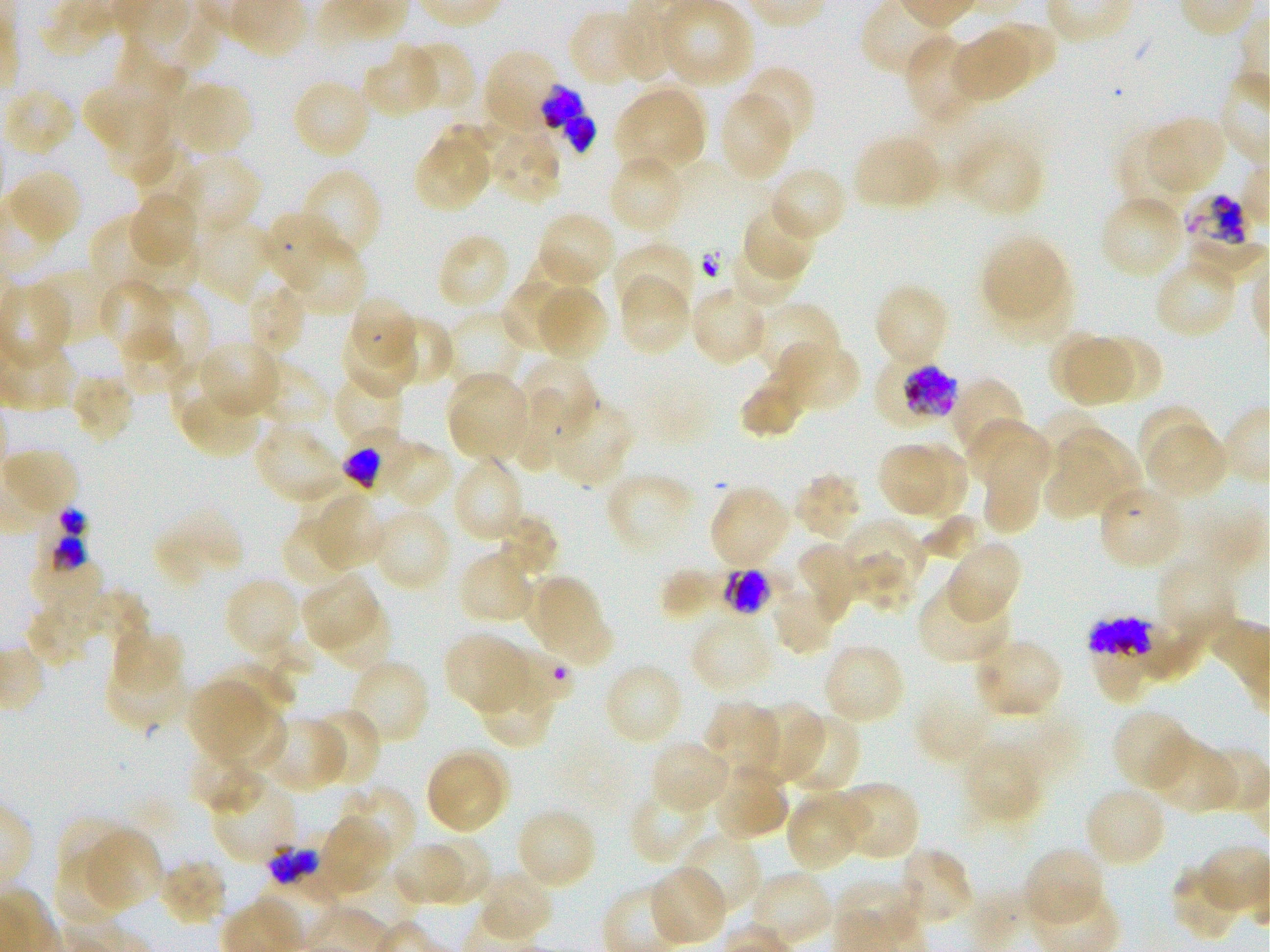 Approximate bounding boxes as (x1, y1, x2, y2) in pixels. Not every red blood cell is marked. A life-cycle stage — or a range of stages, where the recorded stages span more than one — follows each staged infected red blood cell. Locations of infected red blood cells: (541, 84, 597, 153); (876, 357, 961, 429) late trophozoite to early schizont; (342, 431, 407, 492) trophozoite; (38, 507, 89, 571); (722, 568, 772, 617) late trophozoite to early schizont; (1088, 617, 1152, 701) early trophozoite to late schizont. Locations of uninfected red blood cells: (619, 0, 678, 83), (656, 2, 753, 88), (567, 10, 645, 88), (990, 24, 1056, 82), (951, 31, 1033, 102), (904, 35, 978, 123), (116, 38, 187, 119), (405, 39, 476, 113), (362, 48, 440, 119), (484, 49, 562, 134), (738, 65, 816, 147), (291, 78, 372, 160), (173, 82, 253, 156), (84, 83, 171, 154), (615, 86, 707, 173), (3, 87, 76, 158), (719, 92, 794, 181), (914, 104, 996, 190), (1147, 116, 1226, 195), (438, 124, 499, 182), (112, 125, 174, 185), (487, 125, 562, 205), (1115, 127, 1188, 208), (956, 131, 1044, 217), (853, 135, 941, 211), (413, 137, 491, 212), (134, 145, 202, 214), (176, 154, 261, 237), (608, 154, 684, 235), (769, 166, 849, 242), (8, 169, 82, 244), (304, 171, 380, 254), (130, 191, 198, 267), (1099, 194, 1186, 280), (742, 204, 815, 279), (262, 211, 338, 292), (536, 211, 615, 289), (89, 217, 167, 289), (194, 218, 275, 303), (290, 235, 365, 316), (981, 236, 1067, 318), (441, 237, 508, 304), (138, 240, 200, 301), (613, 241, 694, 316), (729, 241, 803, 307), (989, 259, 1074, 342), (1158, 265, 1232, 335), (31, 268, 112, 344), (618, 276, 690, 357), (502, 277, 573, 353), (98, 281, 176, 357), (536, 284, 609, 362), (250, 285, 304, 353), (690, 285, 770, 367), (873, 285, 951, 367), (151, 288, 211, 378), (354, 297, 416, 366), (754, 301, 841, 382), (445, 311, 526, 388), (384, 316, 455, 388), (346, 324, 417, 399), (125, 326, 186, 392), (1050, 332, 1117, 398), (1097, 335, 1161, 400), (1064, 339, 1133, 406), (199, 340, 282, 418), (779, 340, 859, 413), (521, 357, 598, 440), (168, 358, 232, 425), (256, 362, 330, 433), (333, 371, 406, 446), (446, 371, 530, 459), (70, 373, 136, 444), (739, 373, 806, 439), (950, 377, 1026, 461), (450, 387, 522, 456), (184, 395, 260, 454), (552, 399, 634, 487), (1135, 403, 1212, 476), (1040, 408, 1108, 479), (969, 419, 1049, 484), (1147, 422, 1227, 500), (255, 424, 343, 504), (1056, 430, 1143, 515), (981, 439, 1041, 537), (384, 441, 455, 509), (911, 443, 969, 521), (879, 445, 945, 515), (4, 447, 80, 519), (1043, 447, 1119, 521), (453, 455, 526, 543), (604, 472, 694, 556), (793, 473, 863, 541), (709, 485, 791, 568), (1099, 488, 1183, 565), (313, 492, 388, 569), (159, 505, 242, 579), (371, 508, 452, 592), (281, 514, 355, 588), (493, 514, 558, 580), (920, 514, 982, 562), (840, 517, 925, 601), (152, 531, 208, 590), (946, 540, 1023, 621), (793, 542, 857, 622), (458, 548, 536, 626), (852, 550, 917, 615), (1154, 555, 1238, 646), (659, 568, 722, 619), (526, 574, 610, 665), (223, 576, 300, 660), (301, 576, 379, 652), (917, 582, 1011, 665), (771, 585, 839, 656), (85, 589, 149, 651), (24, 602, 93, 668), (1141, 616, 1209, 684), (690, 617, 775, 694), (112, 626, 186, 693), (442, 632, 528, 715), (973, 636, 1065, 719), (256, 638, 315, 704), (821, 643, 906, 726), (345, 657, 431, 747), (103, 659, 189, 730), (213, 661, 295, 722), (603, 661, 684, 747), (478, 672, 556, 750), (186, 680, 264, 760), (913, 687, 991, 765), (750, 698, 823, 784), (213, 701, 287, 773), (703, 702, 781, 784), (310, 707, 384, 788), (1111, 708, 1194, 792), (784, 713, 862, 796), (266, 716, 347, 793), (1149, 737, 1237, 816), (649, 739, 731, 814), (961, 740, 1042, 823), (187, 747, 264, 813), (1201, 747, 1270, 814), (439, 748, 510, 819), (425, 756, 503, 833), (715, 763, 788, 841), (211, 776, 297, 865), (837, 781, 921, 862), (338, 784, 418, 866), (1083, 785, 1166, 868), (628, 788, 709, 866), (785, 791, 865, 871), (515, 808, 598, 889), (55, 815, 133, 890), (318, 816, 391, 893), (83, 828, 163, 911), (680, 832, 762, 917), (422, 835, 491, 904), (392, 840, 466, 908), (896, 847, 975, 928), (1023, 847, 1106, 926), (54, 849, 127, 927), (158, 857, 228, 926), (1171, 863, 1243, 940), (649, 865, 730, 947), (483, 871, 557, 938), (749, 871, 834, 947). Locations of red blood cells of indeterminate infection status: (1182, 192, 1248, 248), (514, 387, 573, 472), (21, 558, 106, 606), (483, 648, 573, 715), (266, 844, 321, 885). Giemsa stain. Image is 1270×952 pixels. Oil immersion, 100x objective (numerical aperture 1.25). Static in-vitro culture of P. falciparum strain 3D7. Blood group of the donor: O+. Thin blood smear. One field from this slide.